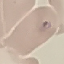 Result: malaria parasites identified. Cell patch, automatically extracted from a larger field of view and resized to 64 × 64 pixels. Thin smear of blood. Giemsa stain. Acquired by smartphone through the microscope eyepiece.